Outline each uninfected red blood cell.
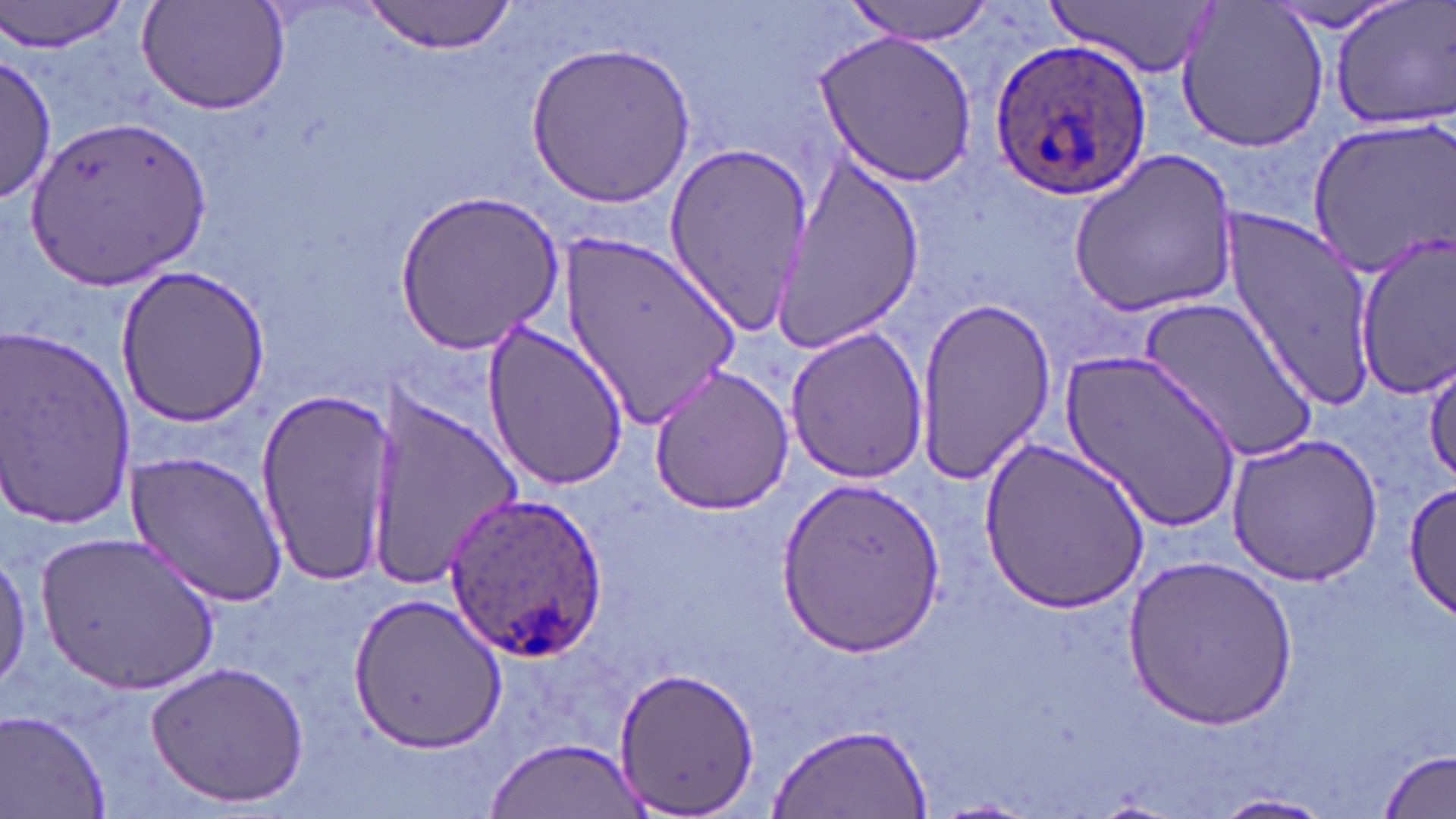
Approximate bounding boxes as (x1,y1)-(x2,y2) corner pairs in pixels.
Uninfected red blood cells: (1,0)-(128,56), (138,0)-(292,118), (844,0)-(995,44), (1047,0)-(1220,77), (1267,0)-(1411,32), (1329,0)-(1456,131), (358,1)-(519,53), (1175,1)-(1330,153), (812,29)-(980,189), (525,41)-(696,206), (0,53)-(55,204), (26,110)-(210,288), (1302,116)-(1453,277), (662,142)-(813,337), (1069,150)-(1239,319), (769,152)-(923,356), (393,188)-(565,352), (1225,208)-(1381,402), (1355,236)-(1456,397), (559,238)-(740,423), (117,265)-(270,425), (1138,295)-(1319,465), (915,296)-(1058,488), (481,319)-(629,490), (0,322)-(138,530), (784,325)-(929,485), (1061,347)-(1242,532), (1422,354)-(1456,489), (646,364)-(797,516), (254,385)-(401,589), (361,393)-(520,585), (1225,433)-(1387,586), (980,437)-(1150,613), (124,449)-(290,610), (774,475)-(947,659), (1403,478)-(1456,622), (39,531)-(223,695), (0,546)-(32,696), (1125,553)-(1297,730), (346,592)-(507,754), (144,658)-(310,808), (610,667)-(760,817), (1,711)-(113,818), (767,722)-(933,819), (486,736)-(642,816), (1380,749)-(1455,819), (1208,792)-(1337,819).

Plasmodium ovale-infected red blood cell locations: (991,36)-(1154,201), (441,492)-(604,664). Slide-level diagnosis: Plasmodium ovale. Optical microscopy. Image is 1456×819 pixels. One field of a larger specimen. 1000x magnification. May-Grünwald-Giemsa-stained preparation. Thin blood film.